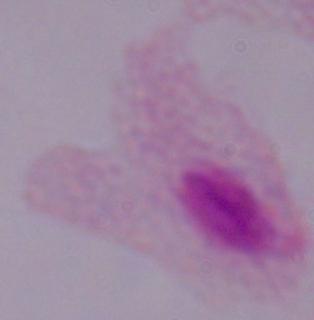

Summary:
  - Identification: trichomonad
  - Magnification: 1000x
  - Modality: micrograph